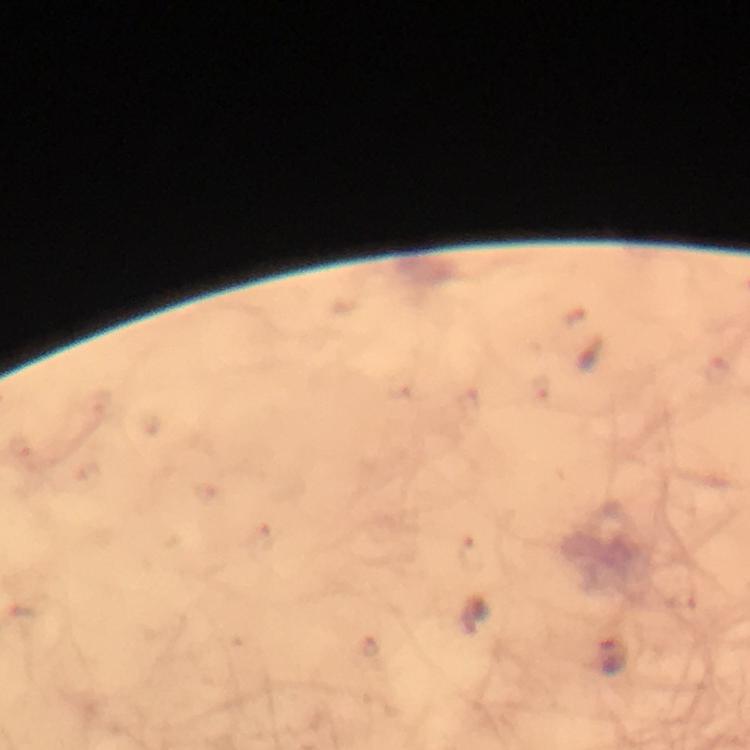 Approximate centers as (x, y) in pixels. Plasmodium parasite locations: (613, 656). Giemsa stain. Photographed with a smartphone mounted on the microscope. Thick blood film. At 100x magnification. Immersion oil was used. Image is 750×750 pixels. From a malaria diagnostic workup. A crop from one field of view.